Comment on the morphology of the red blood cells.
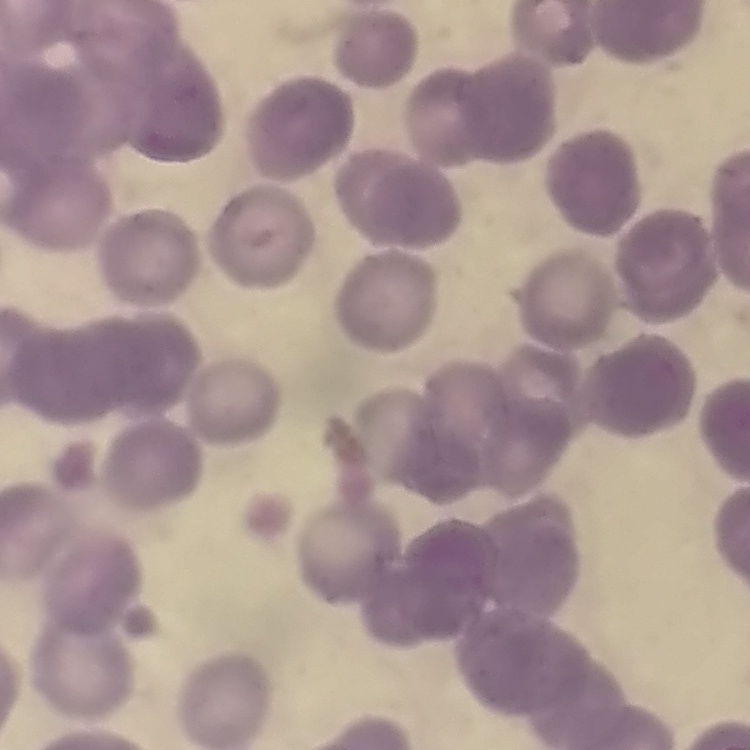
Rouleaux formation.

stain = Field's or Giemsa
preparation = thin peripheral smear
image type = one tile cut from a larger photomicrograph